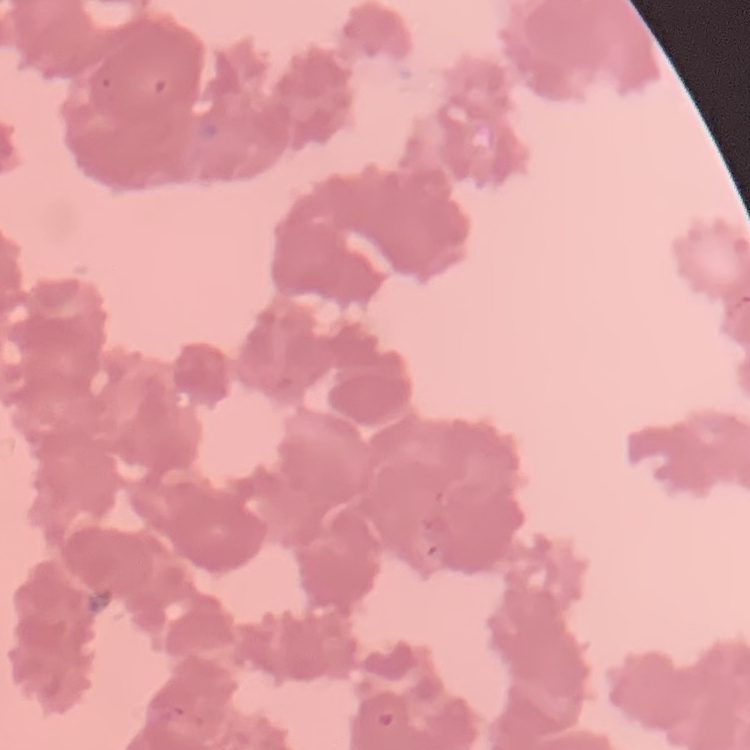

Summary:
  - Red blood cell morphology: rouleaux formation
  - Image type: one tile cut from a larger photomicrograph
  - Preparation: thin blood smear
  - Stain: Field's or Giemsa